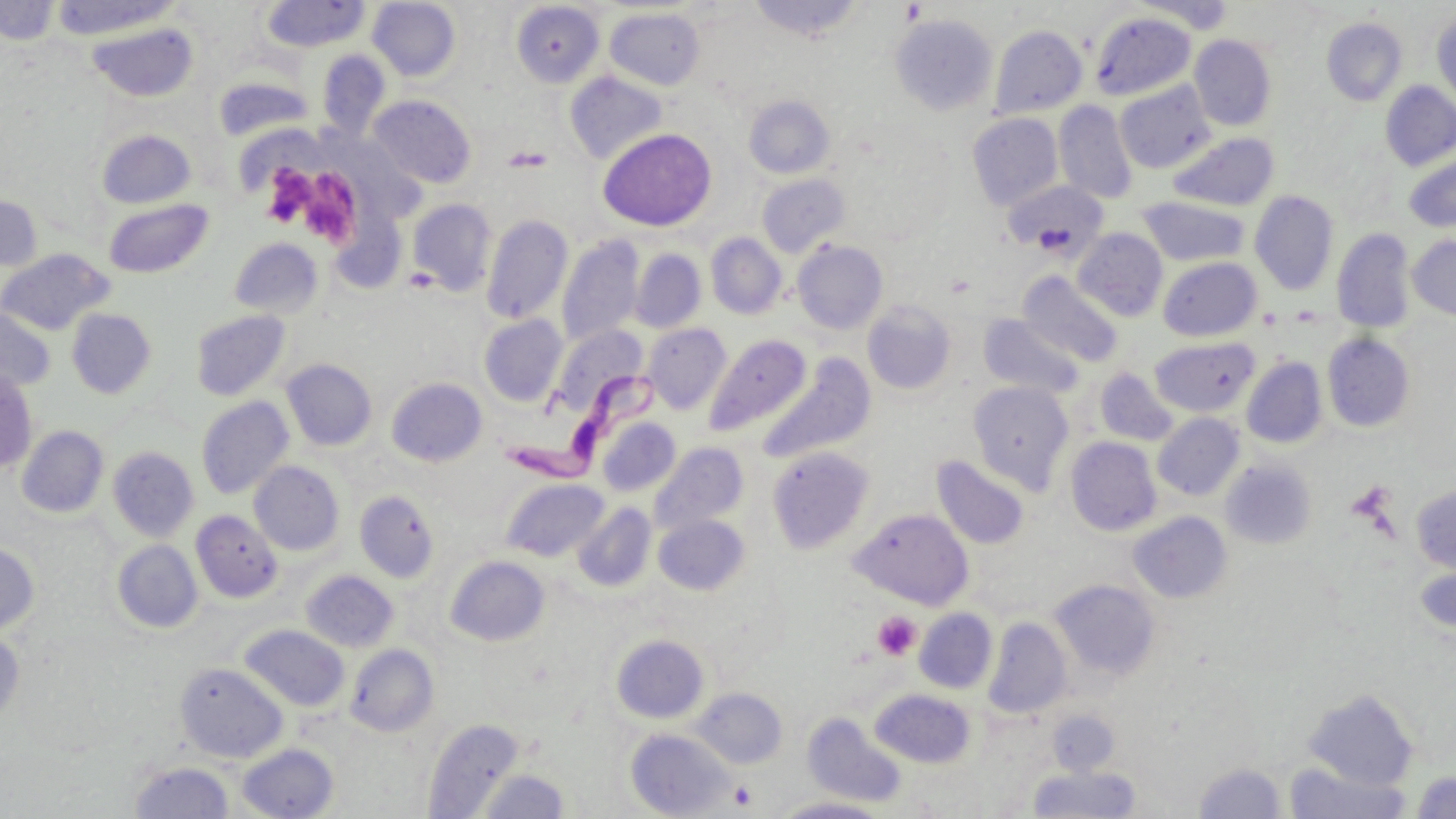
{
  "slide_level_diagnosis": "Trypanosoma brucei",
  "platelet_locations": "approximate bounding boxes as named x1/y1/x2/y2 corners in pixels: (x1=264, y1=169, x2=313, y2=226), (x1=307, y1=174, x2=354, y2=247), (x1=871, y1=611, x2=920, y2=661), (x1=729, y1=780, x2=758, y2=809)",
  "preparation": "thin blood smear",
  "trypanosoma_brucei_locations": "approximate bounding boxes as named x1/y1/x2/y2 corners in pixels: (x1=511, y1=363, x2=673, y2=478)",
  "uninfected_red_blood_cell_locations": "approximate bounding boxes as named x1/y1/x2/y2 corners in pixels: (x1=49, y1=0, x2=182, y2=40), (x1=748, y1=0, x2=866, y2=41), (x1=1135, y1=0, x2=1235, y2=34), (x1=0, y1=1, x2=60, y2=45), (x1=261, y1=1, x2=369, y2=53), (x1=367, y1=1, x2=460, y2=81), (x1=511, y1=3, x2=604, y2=87), (x1=605, y1=7, x2=706, y2=90), (x1=1432, y1=9, x2=1456, y2=107), (x1=1088, y1=11, x2=1196, y2=101), (x1=889, y1=14, x2=999, y2=115), (x1=1321, y1=17, x2=1407, y2=106), (x1=88, y1=22, x2=198, y2=101), (x1=988, y1=24, x2=1087, y2=118), (x1=1189, y1=35, x2=1277, y2=130), (x1=317, y1=49, x2=390, y2=139), (x1=565, y1=72, x2=667, y2=164), (x1=213, y1=75, x2=313, y2=141), (x1=1115, y1=80, x2=1216, y2=174), (x1=1380, y1=81, x2=1456, y2=171), (x1=370, y1=95, x2=476, y2=187), (x1=743, y1=95, x2=835, y2=179), (x1=1054, y1=100, x2=1138, y2=203), (x1=967, y1=113, x2=1063, y2=211), (x1=597, y1=128, x2=717, y2=231), (x1=98, y1=129, x2=196, y2=208), (x1=1168, y1=132, x2=1278, y2=212), (x1=1403, y1=155, x2=1456, y2=232), (x1=757, y1=174, x2=850, y2=257), (x1=1002, y1=179, x2=1109, y2=258), (x1=1249, y1=191, x2=1339, y2=295), (x1=0, y1=195, x2=42, y2=271), (x1=1139, y1=197, x2=1250, y2=267), (x1=104, y1=199, x2=214, y2=278), (x1=407, y1=199, x2=497, y2=296), (x1=330, y1=213, x2=406, y2=294), (x1=481, y1=214, x2=573, y2=325), (x1=1073, y1=228, x2=1168, y2=321), (x1=1331, y1=228, x2=1416, y2=333), (x1=705, y1=233, x2=787, y2=320), (x1=1407, y1=235, x2=1456, y2=321), (x1=228, y1=238, x2=323, y2=319), (x1=558, y1=238, x2=643, y2=346), (x1=793, y1=240, x2=888, y2=334), (x1=0, y1=249, x2=115, y2=335), (x1=630, y1=249, x2=705, y2=332), (x1=1158, y1=257, x2=1261, y2=341), (x1=1019, y1=272, x2=1123, y2=367), (x1=862, y1=301, x2=957, y2=395), (x1=0, y1=306, x2=56, y2=392), (x1=66, y1=308, x2=157, y2=399), (x1=191, y1=310, x2=291, y2=402), (x1=479, y1=314, x2=568, y2=406), (x1=979, y1=314, x2=1084, y2=398), (x1=642, y1=323, x2=731, y2=414), (x1=552, y1=325, x2=647, y2=414), (x1=1322, y1=332, x2=1415, y2=432), (x1=705, y1=334, x2=811, y2=435), (x1=1149, y1=336, x2=1260, y2=417), (x1=759, y1=355, x2=878, y2=463), (x1=1241, y1=357, x2=1328, y2=448), (x1=282, y1=359, x2=377, y2=451), (x1=1094, y1=368, x2=1179, y2=446), (x1=0, y1=370, x2=39, y2=472), (x1=386, y1=378, x2=487, y2=467), (x1=968, y1=381, x2=1074, y2=492), (x1=196, y1=396, x2=294, y2=500), (x1=1153, y1=412, x2=1245, y2=501), (x1=596, y1=416, x2=681, y2=497), (x1=17, y1=425, x2=109, y2=518), (x1=1065, y1=437, x2=1162, y2=536), (x1=649, y1=443, x2=748, y2=535), (x1=107, y1=445, x2=199, y2=542), (x1=767, y1=446, x2=875, y2=553), (x1=932, y1=455, x2=1031, y2=550), (x1=249, y1=460, x2=344, y2=556), (x1=1220, y1=460, x2=1316, y2=549), (x1=500, y1=478, x2=608, y2=561), (x1=1411, y1=483, x2=1456, y2=572), (x1=354, y1=490, x2=439, y2=582), (x1=572, y1=502, x2=656, y2=592), (x1=852, y1=508, x2=974, y2=609), (x1=191, y1=509, x2=282, y2=603), (x1=1129, y1=511, x2=1232, y2=604), (x1=654, y1=515, x2=749, y2=595), (x1=111, y1=539, x2=203, y2=634), (x1=0, y1=541, x2=40, y2=635), (x1=445, y1=555, x2=549, y2=646), (x1=1413, y1=560, x2=1456, y2=635), (x1=301, y1=569, x2=399, y2=652), (x1=1049, y1=578, x2=1161, y2=681), (x1=914, y1=608, x2=998, y2=693), (x1=984, y1=616, x2=1072, y2=719), (x1=240, y1=624, x2=350, y2=711), (x1=0, y1=629, x2=25, y2=725), (x1=611, y1=634, x2=708, y2=723), (x1=346, y1=644, x2=439, y2=736), (x1=174, y1=661, x2=287, y2=762), (x1=691, y1=687, x2=787, y2=768), (x1=1302, y1=687, x2=1419, y2=791), (x1=869, y1=688, x2=977, y2=768), (x1=802, y1=712, x2=908, y2=807), (x1=423, y1=718, x2=524, y2=818), (x1=625, y1=728, x2=734, y2=818), (x1=237, y1=743, x2=339, y2=819), (x1=130, y1=761, x2=234, y2=818), (x1=1194, y1=762, x2=1287, y2=819), (x1=1283, y1=762, x2=1413, y2=819), (x1=1027, y1=765, x2=1141, y2=818), (x1=477, y1=769, x2=569, y2=818), (x1=1411, y1=771, x2=1456, y2=819), (x1=774, y1=796, x2=890, y2=818)",
  "modality": "light microscopy",
  "magnification": "1000x",
  "field_of_view": "single",
  "stain": "May-Grünwald-Giemsa",
  "image_size": "1456×819 pixels"
}